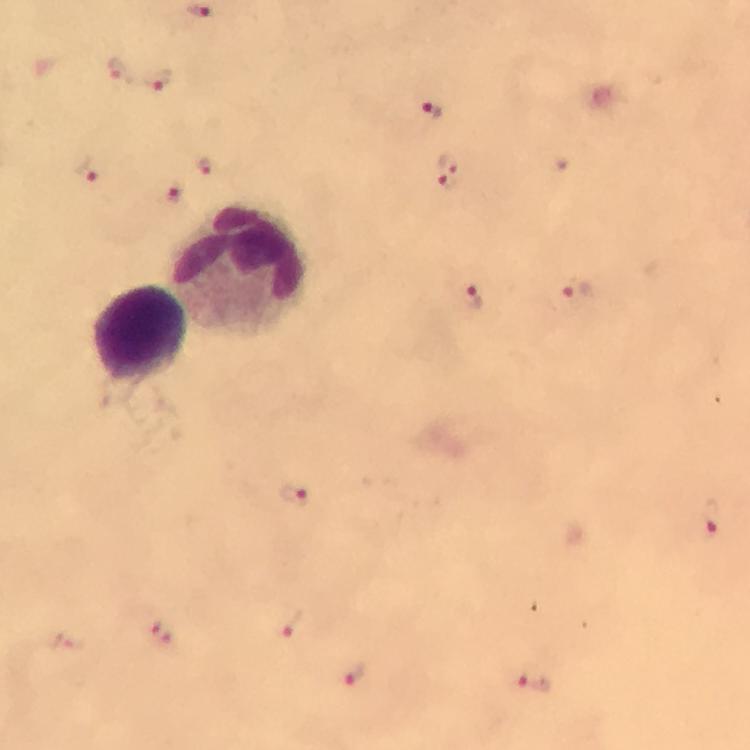
Approximate object centers, in pixels from the top-left corner. Malaria parasite locations: (x=120, y=69), (x=157, y=80), (x=432, y=110), (x=204, y=165), (x=86, y=170), (x=447, y=171), (x=174, y=194), (x=576, y=289), (x=473, y=297), (x=294, y=495), (x=712, y=517), (x=293, y=622), (x=160, y=633), (x=64, y=641), (x=356, y=675), (x=534, y=681). Leukocyte locations: (x=243, y=268), (x=140, y=334). Thick blood film. Immersion oil was used. Image is 750×750 pixels. Photographed through the microscope with a smartphone camera. From a malaria diagnostic workup. Giemsa-stained preparation. At 100x magnification. Cropped region of a single field of view.